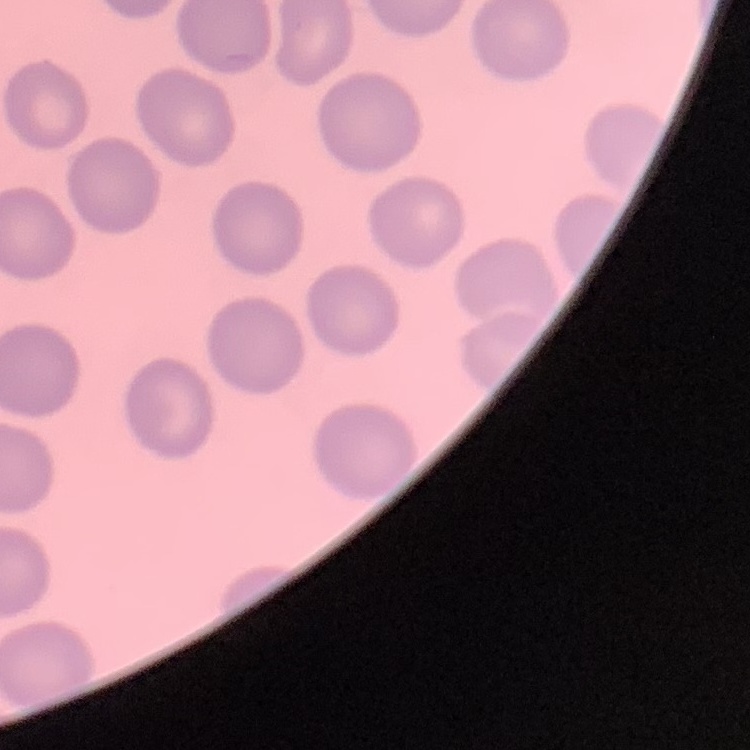
red blood cell morphology = no rouleaux formation
image type = one tile cut from a larger photomicrograph
preparation = thin peripheral smear
stain = Field's or Giemsa